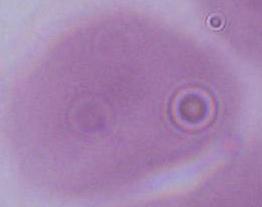

Summary:
  - Identification: erythrocyte
  - Modality: photomicrograph
  - Magnification: 1000x